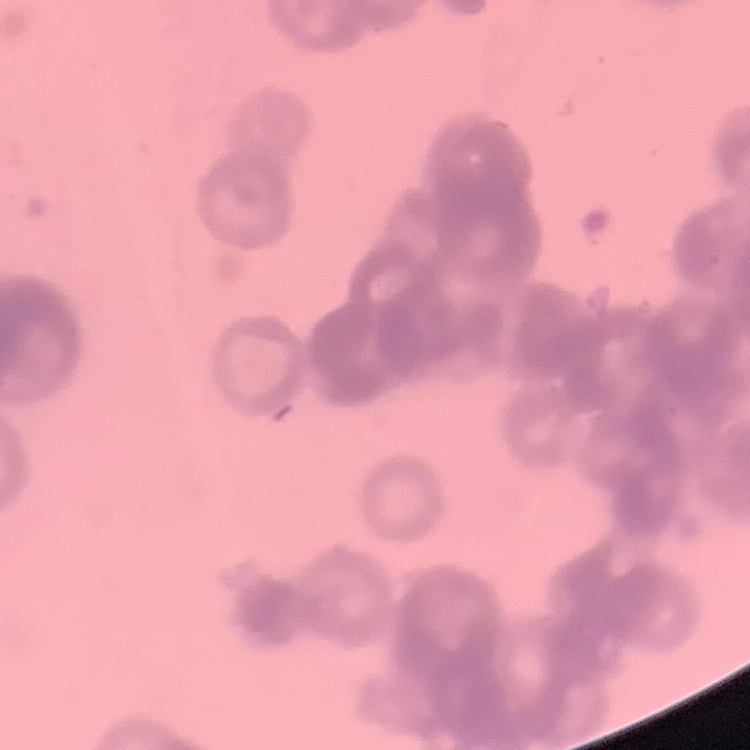

red blood cell morphology = rouleaux formation
stain = Field's or Giemsa
preparation = thin blood film
image type = square crop of a larger photomicrograph